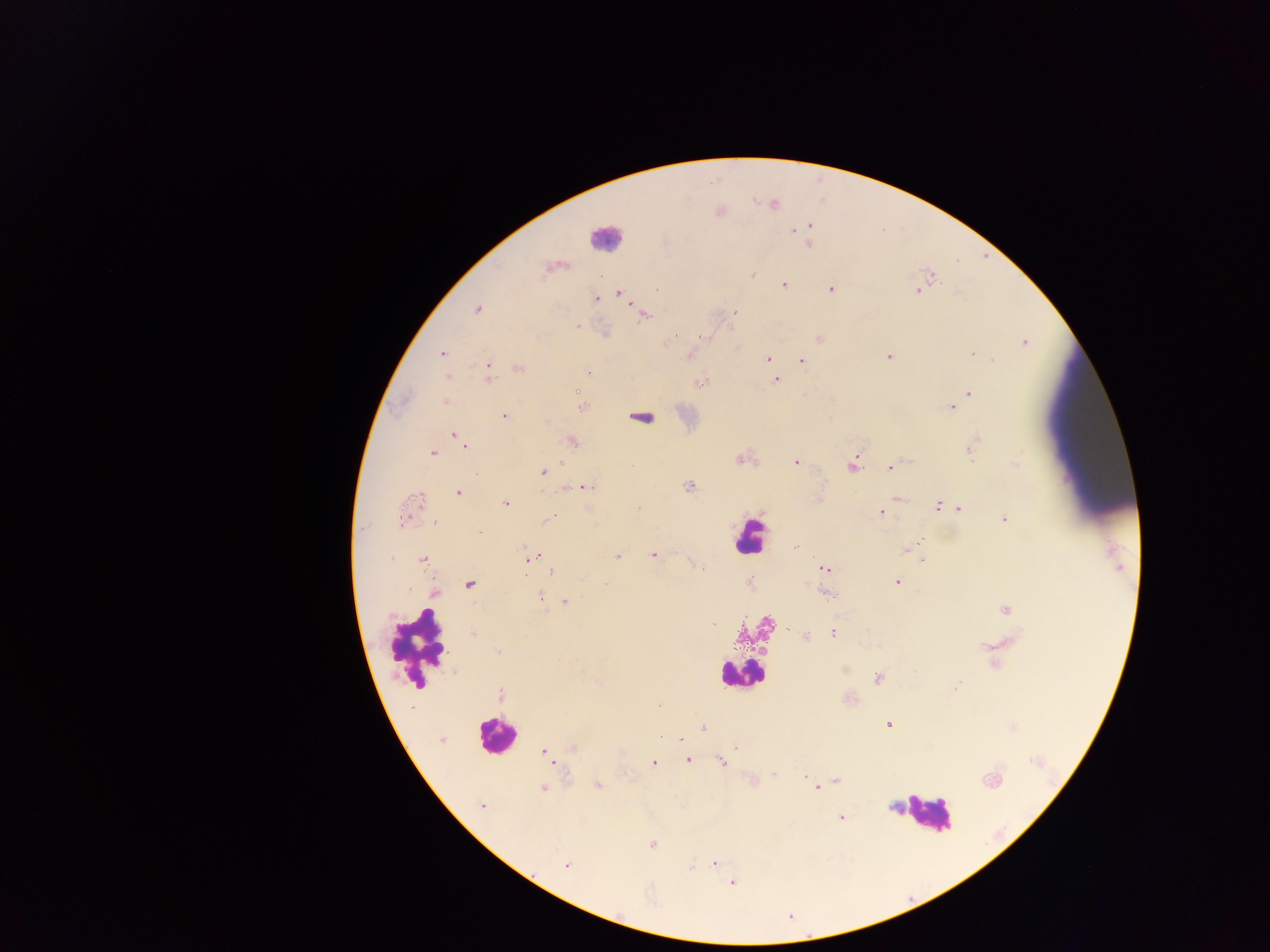

Approximate centers as x y in pixels.
Summary:
  - Plasmodium parasite locations: 774 205; 809 226; 794 231; 809 244; 546 268; 751 275; 931 275; 601 277; 784 285; 830 289; 917 290; 657 291; 620 294; 597 299; 477 309; 734 313; 645 315; 578 326; 706 338; 819 338; 1024 342; 665 344; 442 353; 973 354; 688 356; 888 357; 768 358; 993 360; 801 361; 487 367; 772 367; 519 368; 447 377; 488 378; 775 380; 700 382; 578 391; 969 393; 445 402; 583 407; 951 407; 504 415; 548 421; 455 434; 461 440; 571 441; 465 445; 970 451; 432 453; 739 460; 796 462; 1017 462; 852 465; 890 468; 543 472; 584 486; 688 486; 459 493; 420 498; 898 499; 819 500; 416 502; 506 504; 938 506; 946 507; 638 508; 959 509; 882 512; 549 519; 1004 519; 403 521; 436 522; 479 533; 795 547; 522 548; 906 550; 653 555; 617 556; 533 557; 423 560; 923 560; 547 568; 702 569; 823 569; 552 571; 897 582; 470 584; 606 585; 435 593; 827 594; 540 599; 566 602; 1006 610; 713 624; 789 630; 833 633; 473 634; 805 636; 497 652; 877 678; 599 683; 955 688; 501 695; 659 706; 887 724; 703 728; 660 737; 441 740; 737 747; 573 748; 545 752; 547 756; 688 760; 553 761; 722 762; 654 763; 773 775; 804 776; 837 780; 991 780; 598 785; 817 788; 542 789; 482 806; 842 817; 652 844; 714 863; 566 866; 692 867; 731 883
  - Leukocyte locations: 606 238; 641 414; 749 536; 417 648; 739 674; 495 735; 926 813
  - Country: Ghana
  - Image size: 1270×952 pixels
  - Field of view: single
  - Capture: mobile-phone photograph through a microscope
  - Preparation: thick blood film